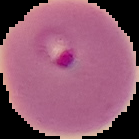
Cell region segmented out of the field of view; the surrounding area is masked to black. From a thin blood film. Image is 139×139 pixels. Malaria status: parasitized.